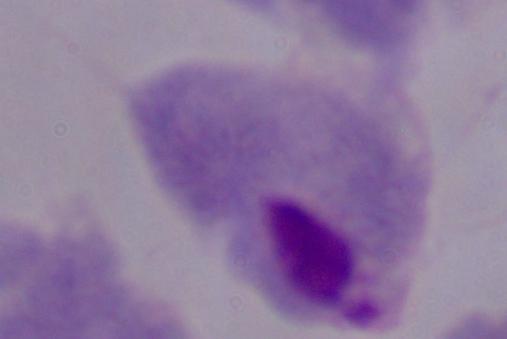
Micrograph. A trichomonad is shown. 1000x magnification.